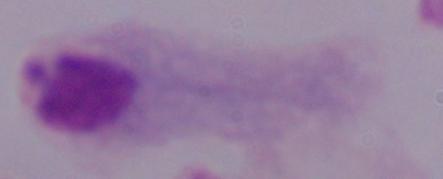 A trichomonad is shown. Photomicrograph. Captured at 1000x magnification.